Comment on the morphology of the red blood cells.
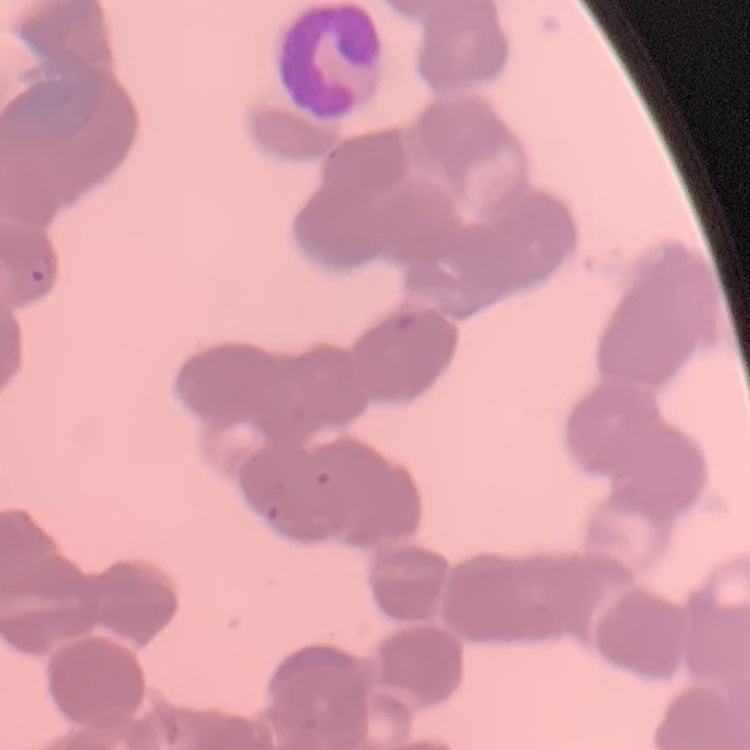

Rouleaux formation.

Summary:
  - Image type: one tile cut from a larger photomicrograph
  - Stain: Field's or Giemsa
  - Preparation: thin blood film